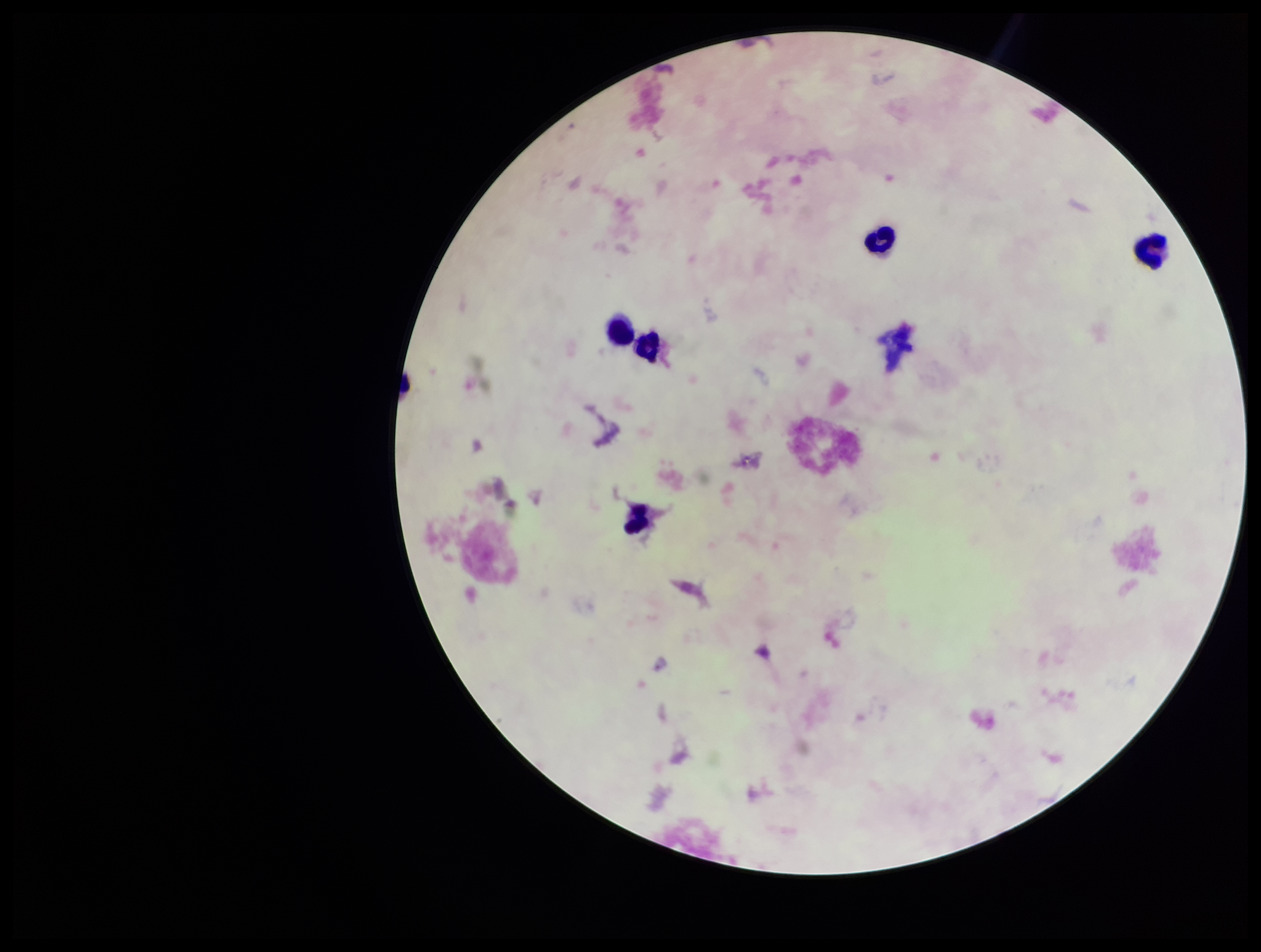
plasmodium_parasites: none detected
species_reported_for_this_patient: Plasmodium falciparum
leukocyte_count: 5
preparation: thick
stain: Giemsa
capture: smartphone photograph through the microscope eyepiece
field_of_view: single
parasite_count: 0
image_size: 1261×952 pixels
patient_malaria_status: positive